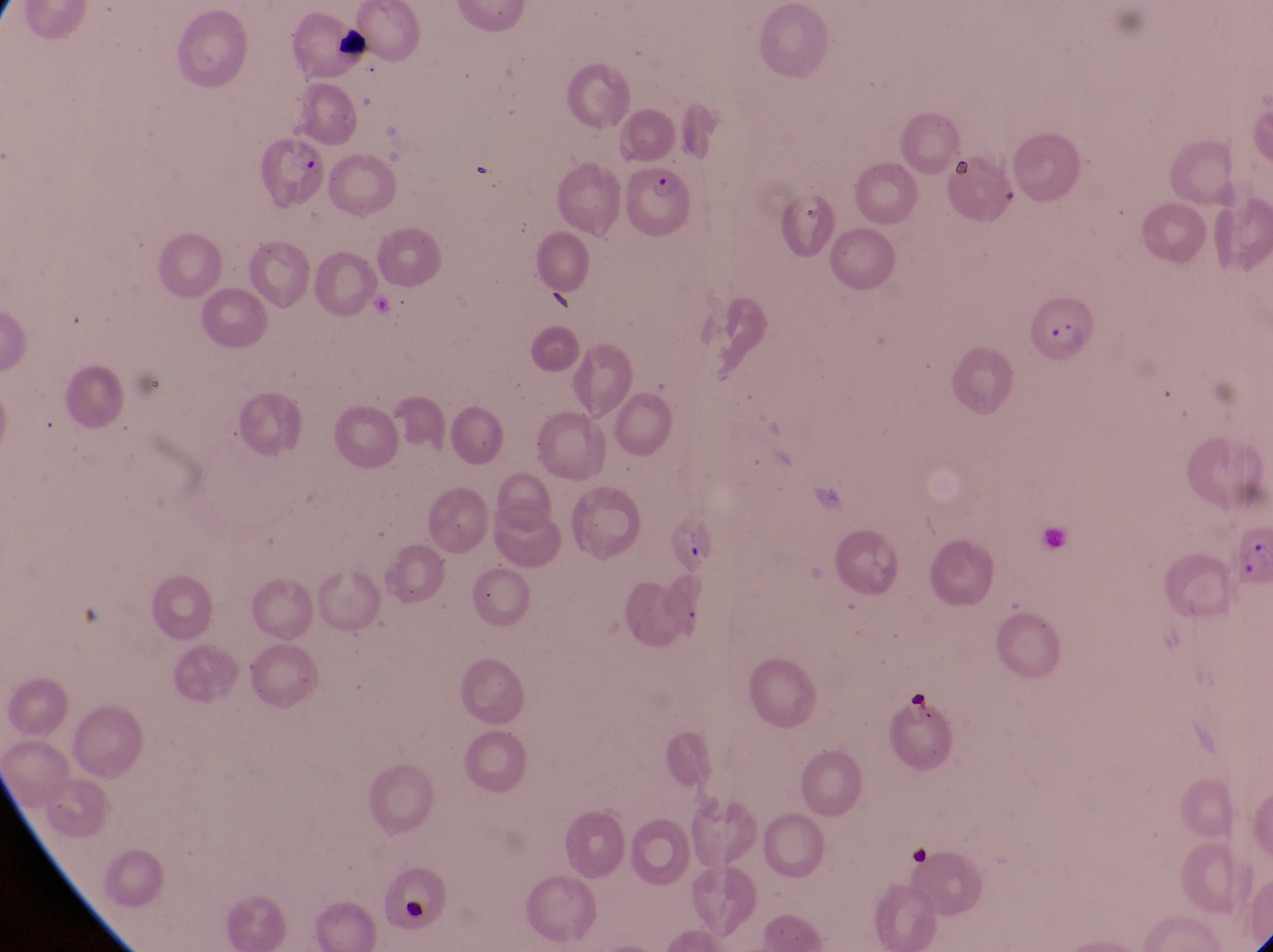

Approximate bounding boxes as {left, top, right, bottom} in pixels.
Summary:
  - Parasitised red blood cell locations: {264, 134, 324, 209}, {619, 160, 702, 240}, {1023, 290, 1098, 365}, {666, 514, 718, 579}
  - Artifact (platelet-like body, stain precipitate, or debris) locations: {334, 27, 376, 59}, {904, 686, 939, 729}, {399, 891, 432, 931}
  - Image size: 1273×952 pixels
  - Country: Uganda
  - Capture: smartphone photograph through the eyepiece of an Olympus CX-23 microscope
  - Field of view: single
  - Preparation: thin blood film
  - Magnification: 1000x